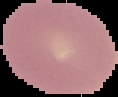
Malaria status: uninfected. From a thin blood film. Image is 118×97 pixels. Segmented cell region on a black background.